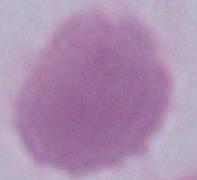

magnification = 1000x
modality = photomicrograph
identification = red blood cell